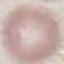

Malaria status: uninfected. Thin blood film. Photographed with a smartphone camera at the microscope eyepiece. Giemsa-stained preparation. Cell patch, automatically extracted from a larger field of view and resized to 64 × 64 pixels.